State which parasite is depicted.
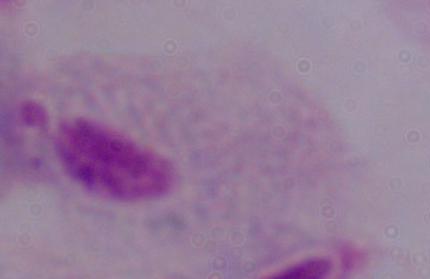
A trichomonad.

magnification: 1000x
modality: photomicrograph